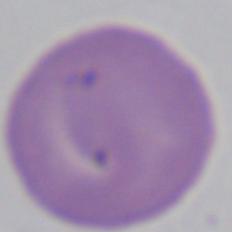

Summary:
  - Magnification: 1000x
  - Modality: micrograph
  - Identification: Babesia